Classify this cell by malaria status.
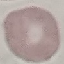

It is uninfected.

Summary:
  - Image type: automatically extracted cell patch, resized to 64 × 64 pixels
  - Stain: Giemsa
  - Capture: smartphone through the microscope eyepiece
  - Preparation: thin blood film